Comment on the morphology of the red blood cells.
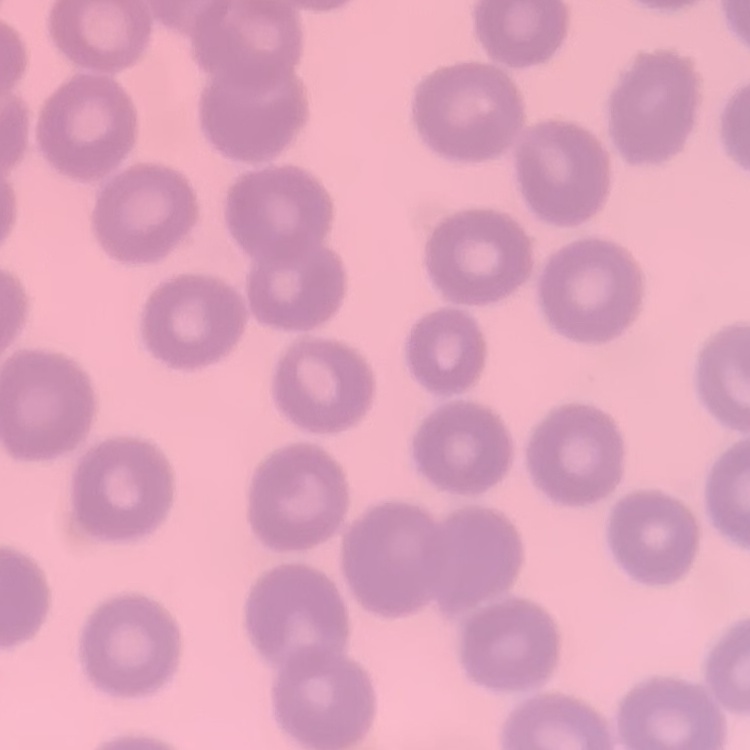

No rouleaux formation.

stain = Field's or Giemsa
image type = one tile cut from a larger photomicrograph
preparation = thin blood film